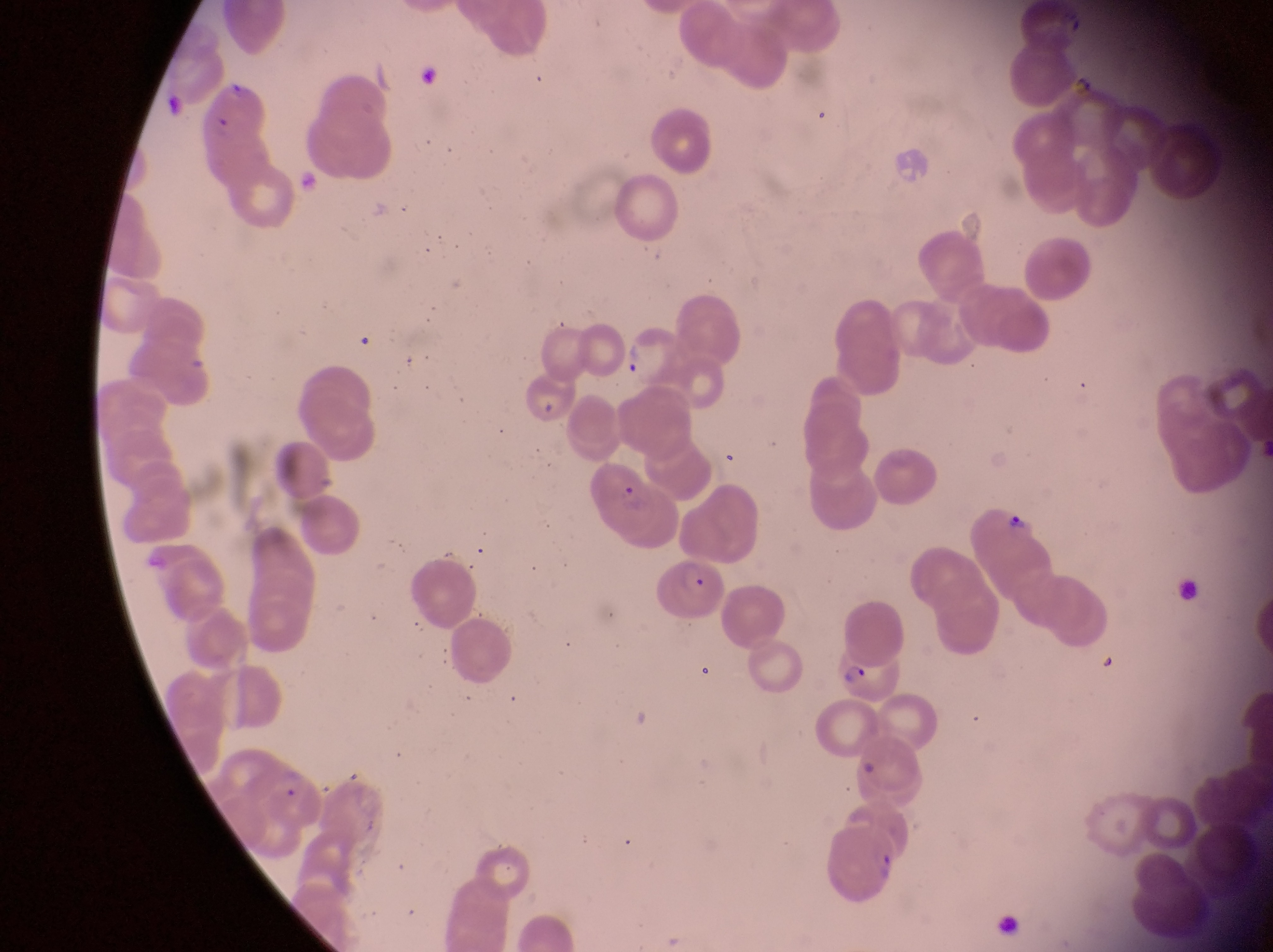

Approximate bounding boxes as (left, top, right, bottom) in pixels.
Summary:
  - Parasitised red blood cell locations: (626, 329, 688, 394), (526, 377, 579, 434), (968, 499, 1046, 562), (656, 557, 725, 622), (824, 649, 899, 709), (829, 817, 901, 905)
  - Field of view: single
  - Preparation: thin blood film
  - Capture: smartphone photograph through the eyepiece of an Olympus CX-23 microscope
  - Country: Uganda
  - Image size: 1273×952 pixels
  - Magnification: 1000x